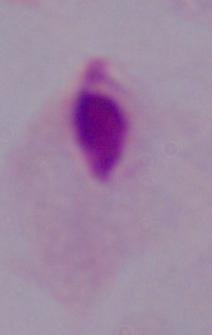

Micrograph. A trichomonad is seen. 1000x magnification.